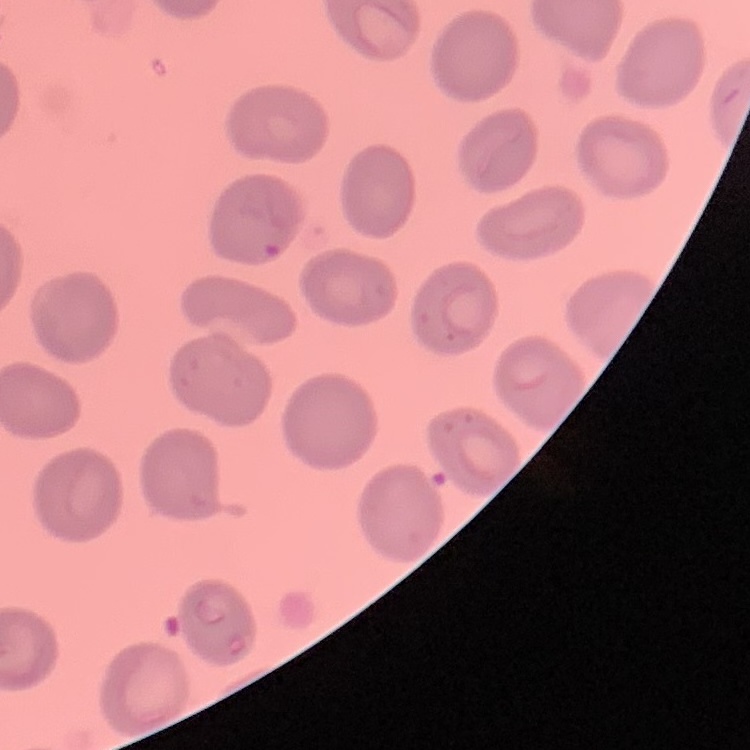

erythrocyte morphology = no rouleaux formation
stain = Field's or Giemsa
image type = one tile cut from a larger photomicrograph
preparation = thin blood smear